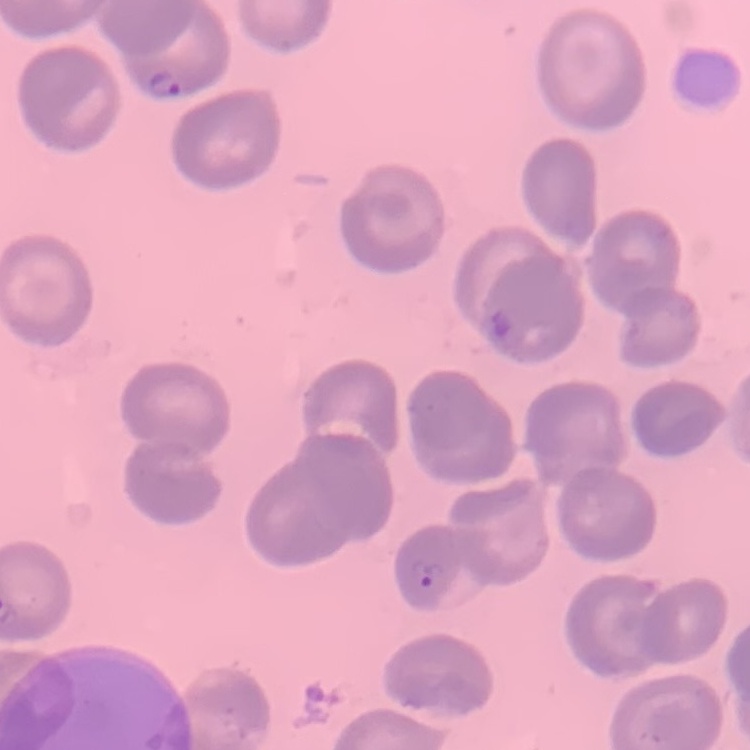

Summary:
  - Red blood cell morphology: no rouleaux formation
  - Image type: square crop of a larger photomicrograph
  - Preparation: thin blood smear
  - Stain: Field's or Giemsa